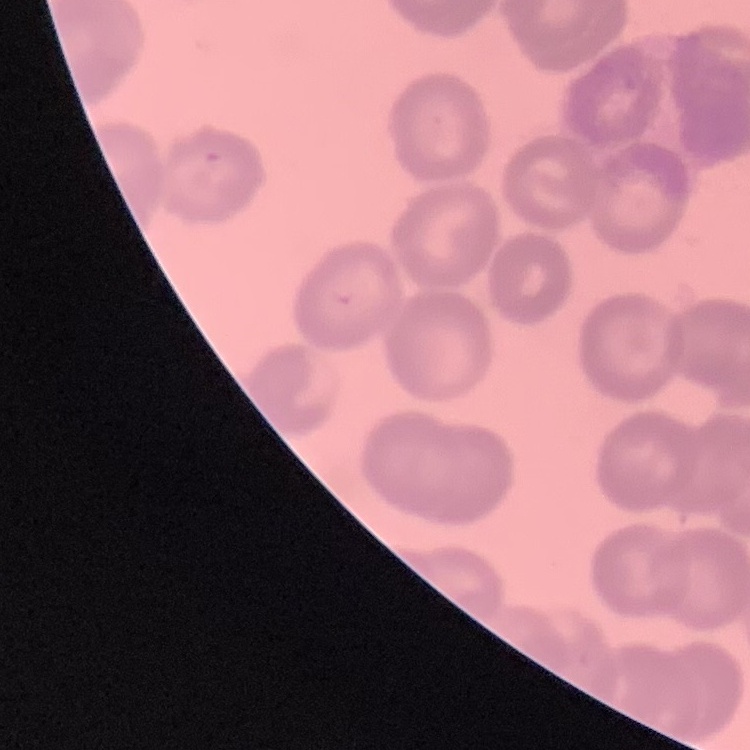
red blood cell morphology = rouleaux formation
stain = Field's or Giemsa
preparation = thin blood film
image type = square crop of a larger photomicrograph